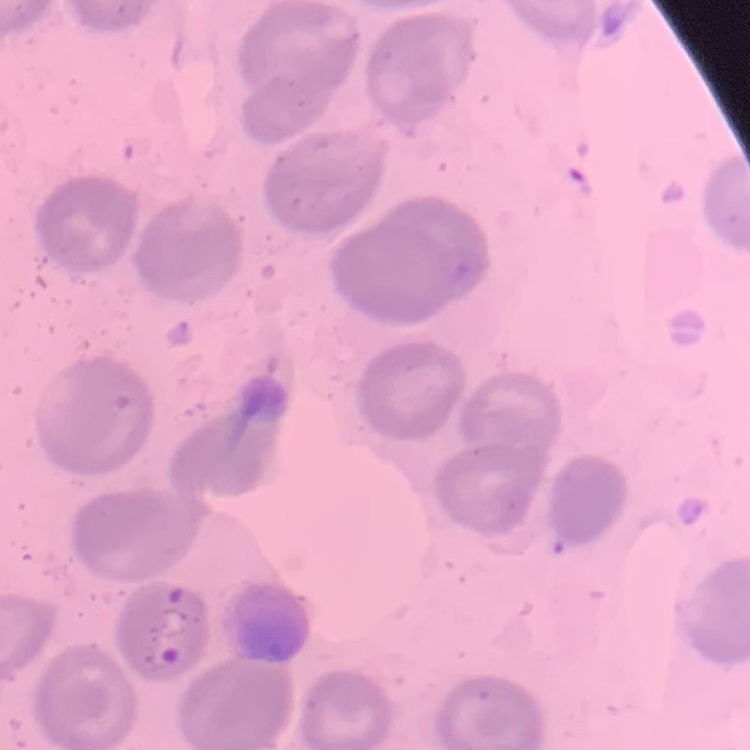

{
  "erythrocyte_morphology": "no rouleaux formation",
  "preparation": "thin peripheral smear",
  "stain": "Field's or Giemsa",
  "image_type": "square crop of a larger photomicrograph"
}